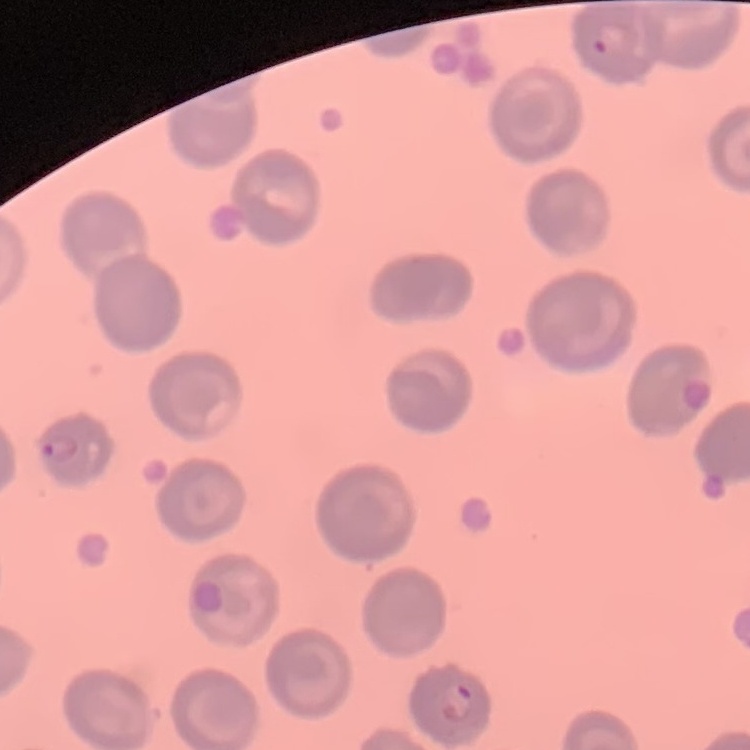

Summary:
  - Erythrocyte morphology: no rouleaux formation
  - Stain: Field's or Giemsa
  - Preparation: thin peripheral smear
  - Image type: square crop of a larger photomicrograph